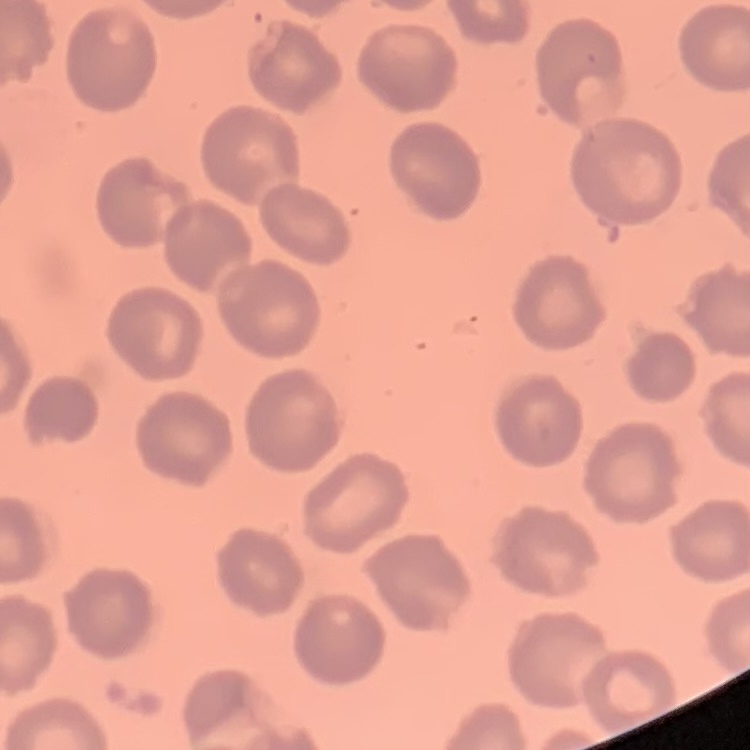 The erythrocytes show no rouleaux formation. Stained with either Field's or Giemsa. One tile cut from a larger photomicrograph. Thin blood film.